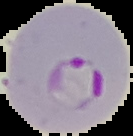
malaria_status: parasitized
image_type: segmented cell region with the area outside set to black
image_size: 133×136 pixels
preparation: thin blood film